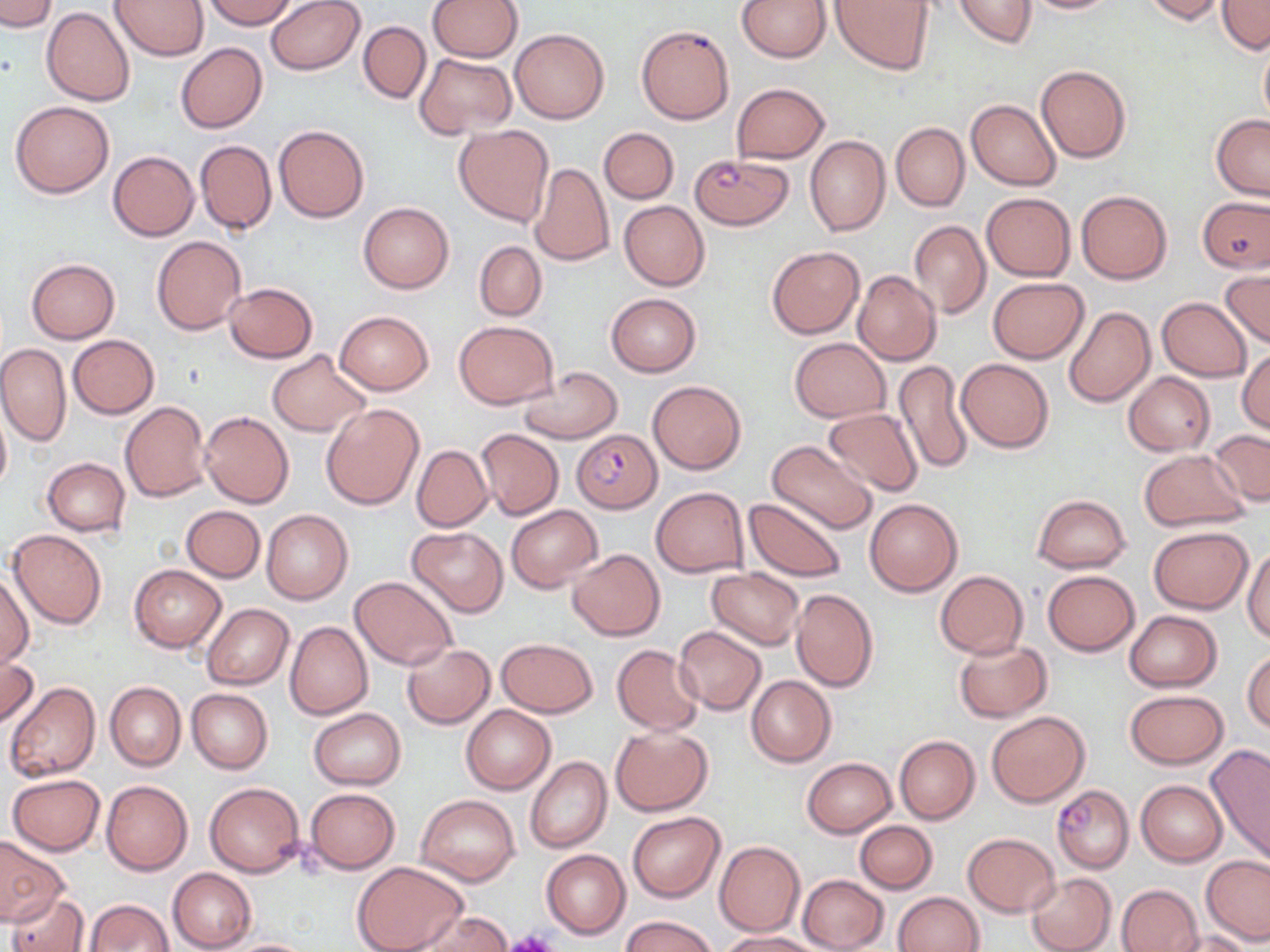
Summary:
  - Coordinate format: approximate bounding boxes as named x1/y1/x2/y2 corners in pixels
  - Plasmodium falciparum-infected red blood cell locations: (x1=690, y1=152, x2=791, y2=230), (x1=573, y1=427, x2=661, y2=512), (x1=1052, y1=785, x2=1135, y2=874)
  - Platelet locations: (x1=502, y1=932, x2=563, y2=952)
  - Uninfected red blood cell locations: (x1=0, y1=0, x2=58, y2=32), (x1=111, y1=0, x2=210, y2=62), (x1=204, y1=0, x2=298, y2=30), (x1=266, y1=0, x2=364, y2=74), (x1=428, y1=0, x2=523, y2=62), (x1=736, y1=0, x2=829, y2=62), (x1=830, y1=0, x2=935, y2=75), (x1=952, y1=0, x2=1037, y2=49), (x1=1017, y1=0, x2=1126, y2=14), (x1=1140, y1=0, x2=1226, y2=24), (x1=1217, y1=0, x2=1270, y2=52), (x1=41, y1=7, x2=135, y2=107), (x1=358, y1=22, x2=430, y2=103), (x1=636, y1=24, x2=735, y2=125), (x1=511, y1=28, x2=609, y2=123), (x1=1258, y1=35, x2=1270, y2=127), (x1=175, y1=43, x2=268, y2=133), (x1=416, y1=54, x2=518, y2=139), (x1=1035, y1=65, x2=1131, y2=164), (x1=731, y1=83, x2=829, y2=163), (x1=967, y1=99, x2=1061, y2=190), (x1=10, y1=100, x2=113, y2=198), (x1=1211, y1=114, x2=1270, y2=199), (x1=891, y1=122, x2=970, y2=211), (x1=274, y1=124, x2=369, y2=222), (x1=454, y1=124, x2=554, y2=226), (x1=599, y1=127, x2=678, y2=203), (x1=805, y1=136, x2=891, y2=237), (x1=195, y1=140, x2=276, y2=234), (x1=107, y1=150, x2=200, y2=241), (x1=529, y1=162, x2=615, y2=267), (x1=1077, y1=190, x2=1172, y2=284), (x1=981, y1=192, x2=1075, y2=281), (x1=1197, y1=197, x2=1270, y2=276), (x1=618, y1=201, x2=710, y2=291), (x1=358, y1=202, x2=455, y2=294), (x1=908, y1=221, x2=991, y2=318), (x1=151, y1=235, x2=247, y2=336), (x1=474, y1=241, x2=546, y2=321), (x1=766, y1=245, x2=864, y2=339), (x1=26, y1=258, x2=120, y2=343), (x1=1221, y1=267, x2=1270, y2=348), (x1=852, y1=271, x2=941, y2=367), (x1=988, y1=277, x2=1089, y2=363), (x1=225, y1=282, x2=317, y2=362), (x1=606, y1=293, x2=700, y2=375), (x1=1156, y1=298, x2=1252, y2=381), (x1=1063, y1=306, x2=1155, y2=407), (x1=335, y1=310, x2=434, y2=396), (x1=454, y1=321, x2=557, y2=408), (x1=69, y1=335, x2=159, y2=419), (x1=789, y1=338, x2=890, y2=422), (x1=0, y1=342, x2=70, y2=446), (x1=1237, y1=348, x2=1270, y2=435), (x1=267, y1=349, x2=368, y2=437), (x1=956, y1=358, x2=1054, y2=453), (x1=894, y1=359, x2=973, y2=475), (x1=516, y1=367, x2=621, y2=443), (x1=1122, y1=373, x2=1215, y2=456), (x1=648, y1=380, x2=746, y2=473), (x1=120, y1=401, x2=212, y2=502), (x1=321, y1=403, x2=424, y2=509), (x1=0, y1=406, x2=11, y2=497), (x1=823, y1=407, x2=922, y2=496), (x1=200, y1=410, x2=294, y2=508), (x1=476, y1=430, x2=564, y2=519), (x1=1207, y1=430, x2=1270, y2=508), (x1=766, y1=440, x2=878, y2=535), (x1=411, y1=444, x2=493, y2=531), (x1=1140, y1=450, x2=1248, y2=532), (x1=40, y1=458, x2=130, y2=537), (x1=651, y1=487, x2=748, y2=578), (x1=1032, y1=495, x2=1130, y2=572), (x1=744, y1=496, x2=847, y2=583), (x1=864, y1=496, x2=964, y2=597), (x1=506, y1=504, x2=602, y2=593), (x1=182, y1=505, x2=265, y2=581), (x1=262, y1=509, x2=353, y2=605), (x1=408, y1=526, x2=508, y2=616), (x1=1149, y1=526, x2=1252, y2=612), (x1=8, y1=529, x2=108, y2=629), (x1=1244, y1=544, x2=1270, y2=642), (x1=567, y1=548, x2=664, y2=640), (x1=129, y1=564, x2=226, y2=652), (x1=707, y1=568, x2=805, y2=649), (x1=1, y1=570, x2=32, y2=670), (x1=935, y1=570, x2=1029, y2=660), (x1=1043, y1=570, x2=1139, y2=656), (x1=350, y1=576, x2=458, y2=670), (x1=791, y1=589, x2=878, y2=691), (x1=202, y1=604, x2=294, y2=690), (x1=1126, y1=610, x2=1220, y2=691), (x1=284, y1=621, x2=373, y2=719), (x1=674, y1=626, x2=766, y2=715), (x1=498, y1=637, x2=597, y2=718), (x1=954, y1=639, x2=1051, y2=723), (x1=402, y1=644, x2=494, y2=729), (x1=611, y1=644, x2=705, y2=735), (x1=1243, y1=650, x2=1270, y2=733), (x1=1, y1=654, x2=41, y2=730), (x1=746, y1=676, x2=836, y2=766), (x1=7, y1=682, x2=101, y2=782), (x1=105, y1=682, x2=186, y2=771), (x1=186, y1=688, x2=272, y2=775), (x1=1124, y1=689, x2=1228, y2=769), (x1=462, y1=705, x2=555, y2=793), (x1=308, y1=709, x2=406, y2=790), (x1=987, y1=711, x2=1089, y2=806), (x1=611, y1=726, x2=713, y2=815), (x1=894, y1=734, x2=980, y2=824), (x1=1206, y1=745, x2=1270, y2=864), (x1=526, y1=756, x2=611, y2=854), (x1=801, y1=757, x2=897, y2=838), (x1=6, y1=774, x2=106, y2=855), (x1=101, y1=780, x2=193, y2=875), (x1=1136, y1=780, x2=1226, y2=866), (x1=204, y1=781, x2=305, y2=878), (x1=305, y1=787, x2=400, y2=874), (x1=415, y1=794, x2=520, y2=885), (x1=628, y1=812, x2=724, y2=901), (x1=855, y1=820, x2=936, y2=893), (x1=963, y1=833, x2=1060, y2=916), (x1=0, y1=834, x2=69, y2=926), (x1=714, y1=841, x2=805, y2=936), (x1=541, y1=849, x2=631, y2=938), (x1=1202, y1=854, x2=1270, y2=944), (x1=352, y1=862, x2=469, y2=952), (x1=169, y1=867, x2=257, y2=952), (x1=1025, y1=872, x2=1116, y2=952), (x1=798, y1=874, x2=888, y2=952), (x1=1116, y1=883, x2=1205, y2=952), (x1=7, y1=891, x2=89, y2=952), (x1=894, y1=891, x2=984, y2=952), (x1=84, y1=898, x2=173, y2=950), (x1=412, y1=911, x2=511, y2=952), (x1=623, y1=916, x2=715, y2=952), (x1=720, y1=931, x2=822, y2=952), (x1=1170, y1=931, x2=1256, y2=952), (x1=217, y1=937, x2=319, y2=952)
  - Slide-level diagnosis: Plasmodium falciparum
  - Field of view: single
  - Image size: 1270×952 pixels
  - Modality: light microscopy
  - Preparation: thin blood film
  - Magnification: 1000x
  - Stain: May-Grünwald-Giemsa